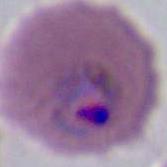 Captured at either 400x or 1000x magnification. Photomicrograph. A Plasmodium parasite is shown.